State which parasite is depicted.
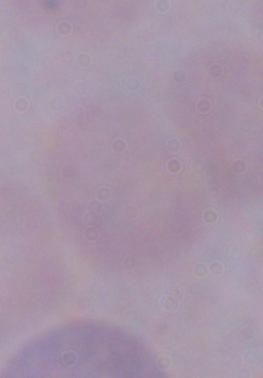

This is a trypanosome.

modality = micrograph
magnification = 1000x